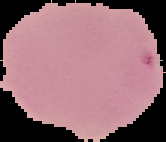 Malaria status: uninfected. Segmented cell region on a black background. Image is 166×142 pixels. From a thin blood film.